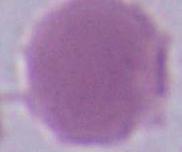

Micrograph. An erythrocyte is seen. 1000x magnification.